Describe the morphology of the erythrocytes.
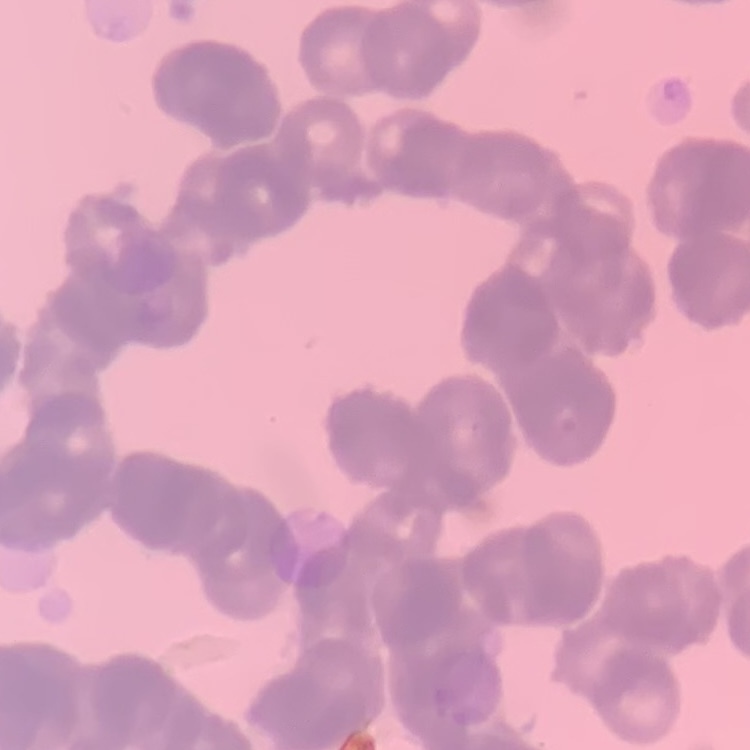

Rouleaux formation.

preparation = thin peripheral smear
stain = Field's or Giemsa
image type = one tile cut from a larger photomicrograph